Give the extent of all Plasmodium falciparum-infected red blood cells.
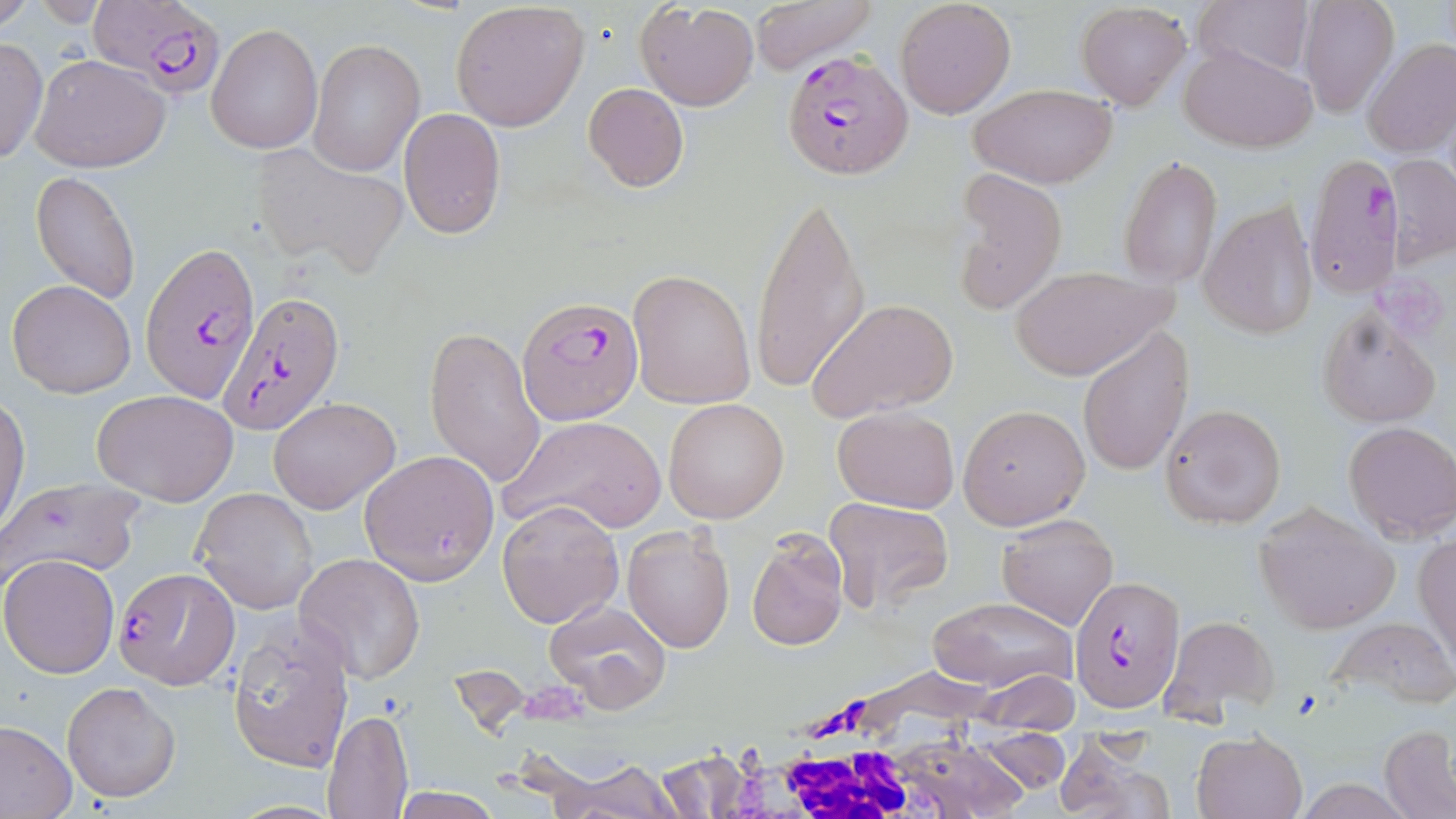
Approximate bounding boxes as (x1,y1)-(x2,y2) corner pairs in pixels.
Plasmodium falciparum-infected red blood cells: (88,2)-(224,96), (780,49)-(912,182), (1308,145)-(1400,298), (141,241)-(260,404), (221,291)-(344,438), (515,297)-(642,427), (111,566)-(238,688), (1069,575)-(1187,714).

{
  "slide_level_diagnosis": "Plasmodium falciparum",
  "white_blood_cell_locations": "approximate bounding boxes as (x1,y1)-(x2,y2) corner pairs in pixels: (698,689)-(1045,819)",
  "modality": "light microscopy",
  "uninfected_red_blood_cell_locations": "approximate bounding boxes as (x1,y1)-(x2,y2) corner pairs in pixels: (0,0)-(35,32), (748,0)-(876,73), (1193,0)-(1312,79), (635,1)-(760,111), (894,1)-(1016,117), (1075,1)-(1193,111), (1298,2)-(1400,116), (450,4)-(591,133), (206,24)-(322,155), (0,37)-(48,166), (309,38)-(424,178), (1361,38)-(1456,157), (1179,42)-(1317,150), (30,54)-(171,173), (583,82)-(690,193), (968,82)-(1117,188), (398,109)-(506,239), (252,145)-(409,276), (1119,153)-(1223,290), (1385,153)-(1456,266), (947,169)-(1066,314), (29,170)-(141,305), (753,184)-(870,400), (1199,200)-(1317,339), (1007,262)-(1176,380), (629,269)-(755,408), (7,279)-(136,399), (807,297)-(958,421), (1319,306)-(1441,428), (424,322)-(545,491), (1078,324)-(1194,477), (91,390)-(239,505), (0,396)-(29,534), (269,396)-(401,514), (663,398)-(788,523), (1161,403)-(1285,529), (958,404)-(1090,529), (832,406)-(959,512), (501,413)-(667,535), (1344,422)-(1456,542), (358,449)-(499,584), (0,476)-(145,588), (192,487)-(319,614), (824,497)-(953,611), (497,499)-(624,629), (1251,503)-(1399,634), (995,514)-(1119,629), (622,525)-(735,653), (747,529)-(850,651), (1416,530)-(1456,666), (0,553)-(120,676), (295,553)-(427,685), (928,598)-(1077,691), (542,599)-(671,712), (1161,614)-(1280,719), (226,616)-(355,775), (1330,616)-(1456,709), (978,669)-(1080,730), (62,681)-(180,803), (322,708)-(414,818), (0,720)-(76,818), (1379,725)-(1456,819), (973,730)-(1071,792), (1192,730)-(1308,819), (1051,734)-(1168,819), (656,747)-(752,816), (553,761)-(685,819), (388,789)-(503,819)",
  "stain": "May-Grünwald-Giemsa",
  "preparation": "thin blood film",
  "image_size": "1456×819 pixels",
  "magnification": "1000x",
  "field_of_view": "one of a larger specimen"
}